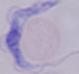

Summary:
  - Magnification: 1000x
  - Identification: trypanosome
  - Modality: micrograph